Point out each malaria parasite.
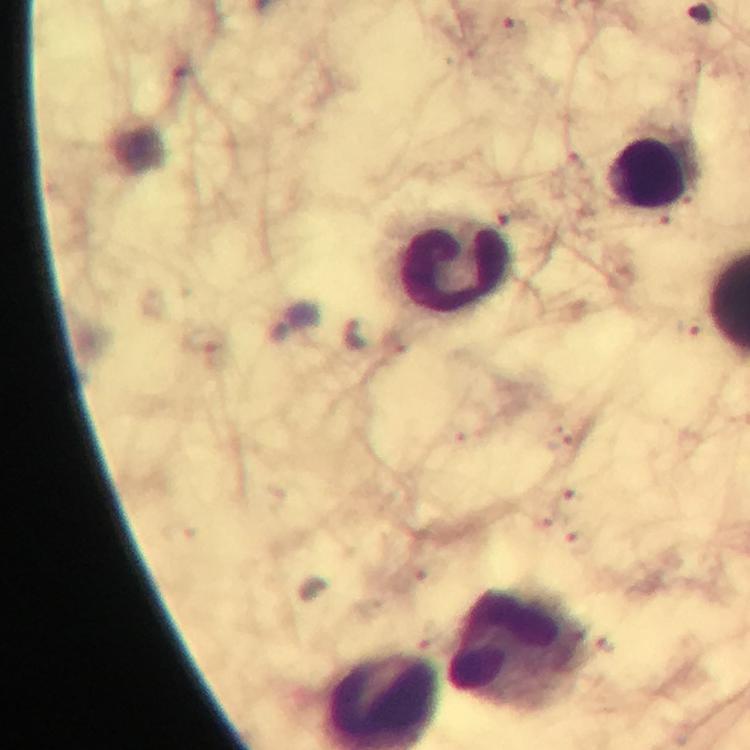

Approximate centers as [x, y] in pixels.
Malaria parasites: [697, 14], [513, 31], [356, 335], [565, 500], [581, 543].

magnification = 100x
immersion oil = applied
preparation = thick blood film
context = from a malaria diagnostic workup
leukocyte locations = approximate centers as [x, y] in pixels: [648, 178], [456, 265], [515, 645]
cropped from = a single field of view
image size = 750×750 pixels
capture = smartphone photograph through a microscope
stain = Giemsa